Name the parasite shown.
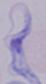
A trypanosome.

Photomicrograph. Captured at 1000x magnification.